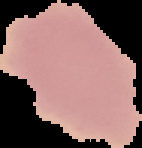
Image is 142×148 pixels. Malaria status: uninfected. From a thin blood film. The area outside the segmented cell region is set to black.